Locate every malaria parasite.
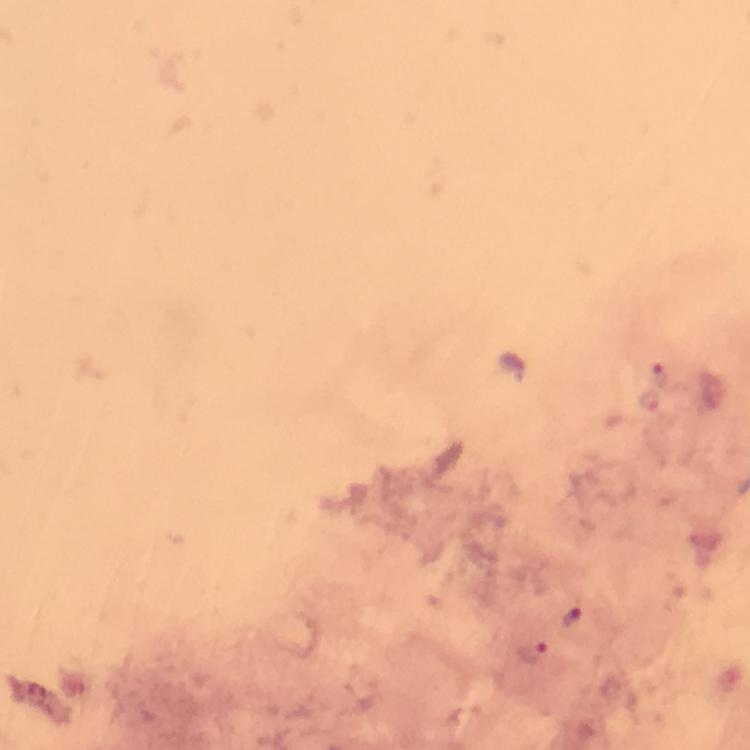

Approximate centers as {x, y} in pixels.
Malaria parasites: {658, 374}, {649, 401}, {572, 617}, {531, 651}.

Summary:
  - Context: from a malaria diagnostic workup
  - Cropped from: one field of view
  - Preparation: thick smear
  - Image size: 750×750 pixels
  - Stain: Giemsa
  - Magnification: 100x
  - Immersion oil: applied
  - Capture: smartphone camera through the microscope